Describe the morphology of the erythrocytes.
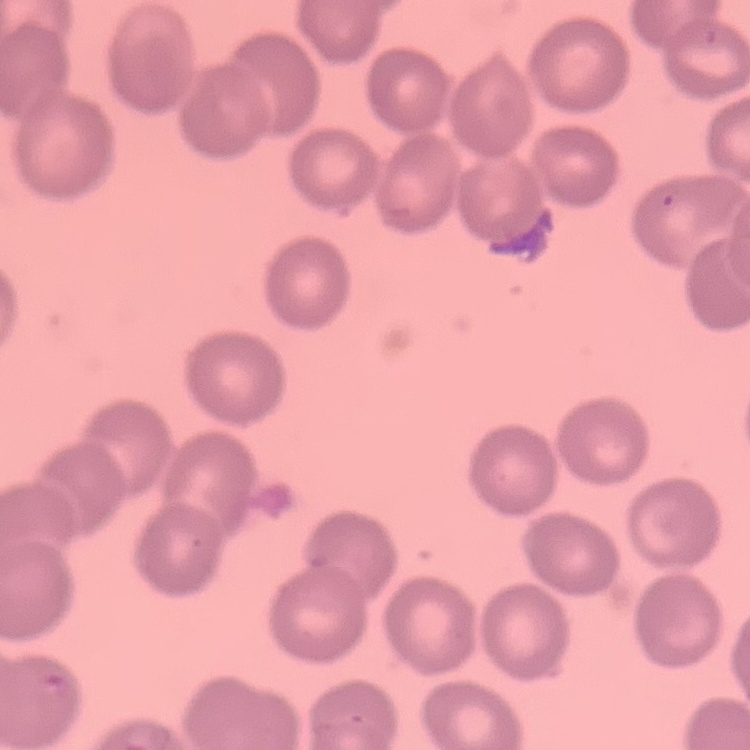

No rouleaux formation.

Thin blood smear. Field's or Giemsa stain. One tile cut from a larger photomicrograph.